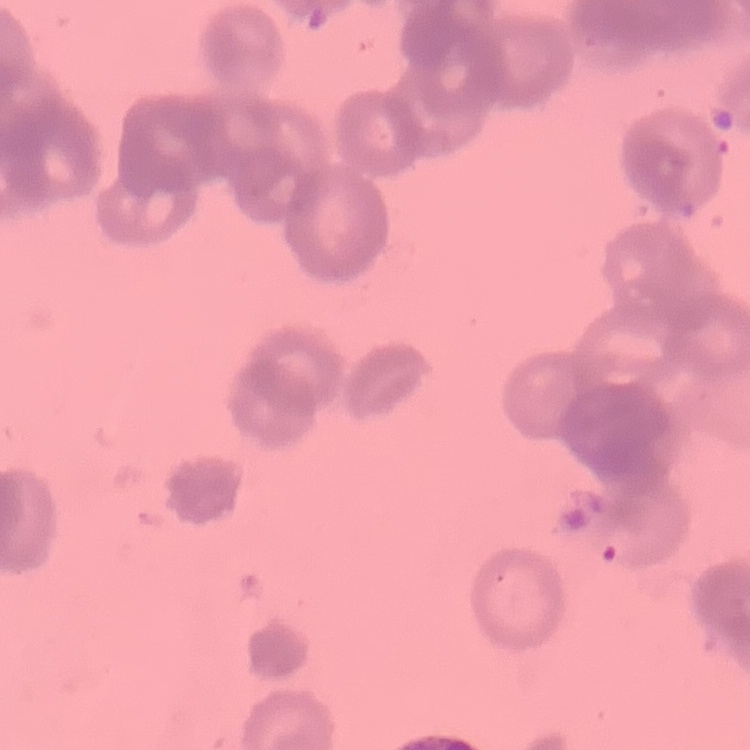
Summary:
  - Erythrocyte morphology: rouleaux formation
  - Image type: one tile cut from a larger photomicrograph
  - Preparation: thin blood smear
  - Stain: Field's or Giemsa